Name the blood parasite species.
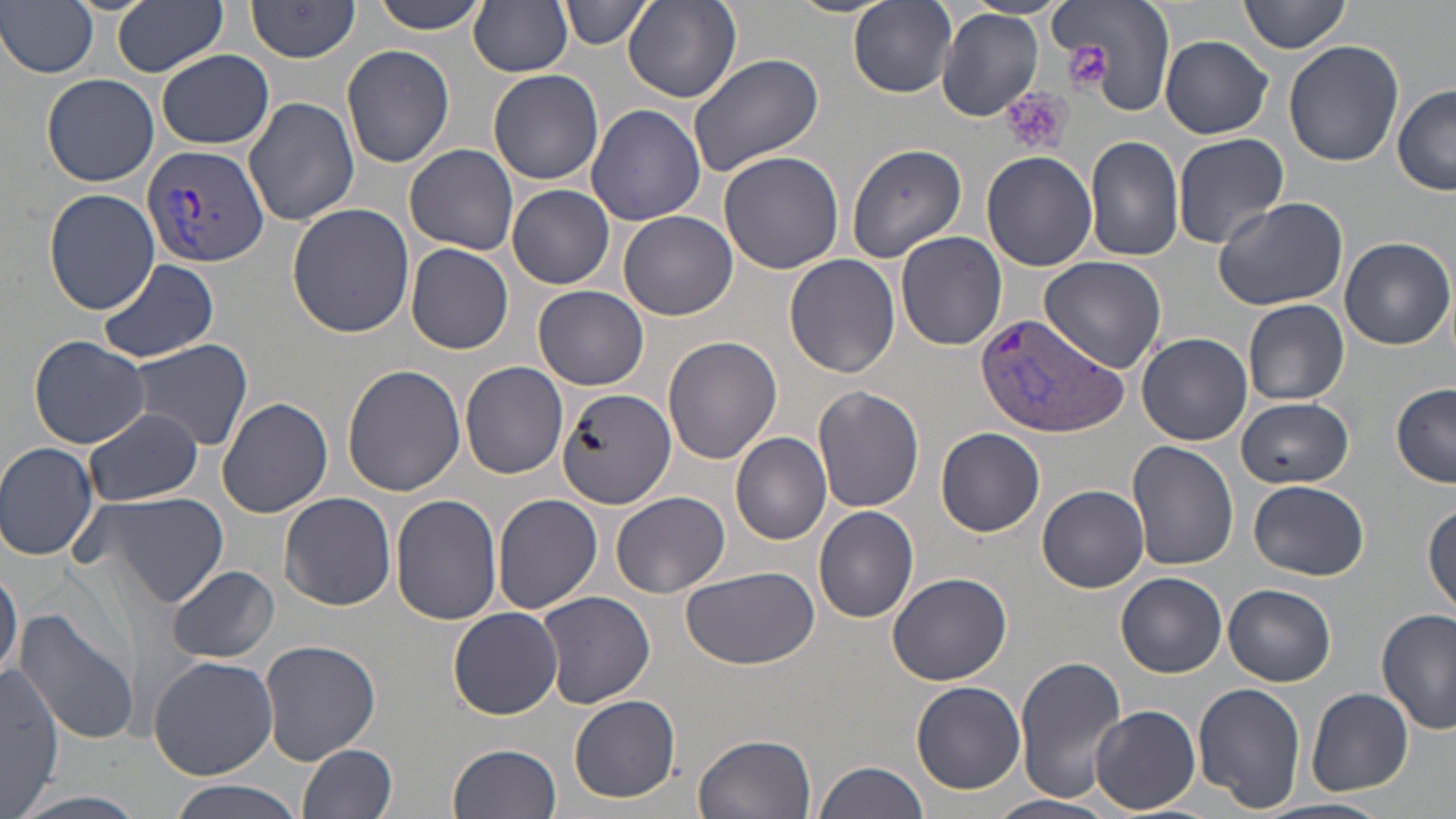

Plasmodium vivax.

platelet locations = approximate bounding boxes as (x1, y1, x2, y2) in pixels: (1066, 43, 1112, 92), (1001, 88, 1073, 157)
stain = May-Grünwald-Giemsa
preparation = thin blood smear
image size = 1456×819 pixels
uninfected red blood cell locations = approximate bounding boxes as (x1, y1, x2, y2) in pixels: (0, 0, 100, 78), (114, 0, 228, 76), (246, 0, 362, 62), (369, 0, 488, 33), (561, 0, 649, 49), (850, 0, 956, 97), (1051, 0, 1177, 116), (1239, 0, 1349, 55), (469, 1, 575, 76), (126, 2, 247, 140), (624, 2, 742, 103), (936, 7, 1044, 124), (1160, 36, 1273, 137), (1283, 39, 1403, 168), (341, 43, 454, 168), (157, 49, 275, 149), (686, 51, 826, 175), (487, 69, 604, 185), (42, 72, 159, 187), (1392, 86, 1456, 196), (244, 98, 360, 227), (586, 104, 706, 226), (1172, 132, 1289, 248), (1085, 135, 1185, 262), (844, 142, 968, 263), (405, 143, 519, 254), (719, 151, 844, 275), (981, 151, 1098, 271), (507, 184, 615, 289), (43, 188, 159, 316), (1212, 194, 1349, 313), (287, 204, 415, 338), (619, 211, 737, 320), (896, 231, 1007, 350), (1339, 237, 1454, 351), (407, 243, 514, 355), (782, 246, 1015, 363), (784, 253, 901, 377), (1038, 254, 1166, 372), (97, 259, 220, 363), (534, 285, 650, 390), (1244, 299, 1349, 405), (1137, 332, 1252, 445), (28, 334, 150, 448), (662, 335, 782, 463), (122, 339, 254, 452), (460, 361, 569, 478), (342, 365, 466, 497), (1391, 384, 1456, 486), (813, 385, 924, 513), (557, 388, 677, 511), (1235, 395, 1356, 488), (217, 396, 335, 517), (84, 407, 202, 505), (936, 427, 1045, 536), (730, 431, 832, 545), (0, 442, 101, 562), (1128, 442, 1240, 571), (1248, 479, 1370, 581), (1039, 485, 1149, 593), (87, 489, 229, 609), (609, 490, 729, 599), (280, 492, 396, 610), (492, 494, 604, 617), (391, 495, 502, 626), (1424, 502, 1456, 619), (814, 506, 920, 623), (0, 558, 21, 685), (168, 566, 279, 663), (680, 566, 818, 670), (886, 572, 1014, 687), (1115, 572, 1227, 678), (1224, 584, 1337, 685), (537, 590, 656, 709), (447, 607, 562, 719), (1375, 607, 1454, 737), (14, 608, 140, 745), (260, 637, 381, 764), (148, 654, 278, 779), (1015, 656, 1126, 803), (0, 665, 63, 812), (912, 681, 1026, 794), (1192, 683, 1306, 811), (1305, 687, 1414, 797), (569, 694, 680, 802), (1091, 705, 1200, 814), (695, 732, 817, 819), (449, 742, 563, 819), (299, 743, 399, 819), (813, 759, 930, 819), (162, 780, 308, 819), (986, 795, 1116, 819), (1256, 798, 1390, 819)
Plasmodium vivax-infected red blood cell locations = approximate bounding boxes as (x1, y1, x2, y2) in pixels: (141, 141, 274, 267), (975, 311, 1130, 440)
magnification = 1000x
modality = optical microscopy
field of view = one of a larger specimen